Classify this cell by malaria status.
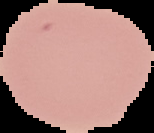
It is uninfected.

Summary:
  - Image size: 154×133 pixels
  - Image type: segmented cell region on a black background
  - Preparation: thin blood film